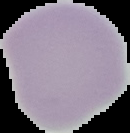 Malaria status: uninfected. Image is 130×133 pixels. From a thin blood smear. Segmented cell region on a black background.